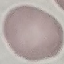

Malaria status: uninfected. Cell patch, automatically extracted from a larger field of view and resized to 64 × 64 pixels. Giemsa stain. Acquired by smartphone through the microscope eyepiece. Thin blood smear.